Point out each leukocyte.
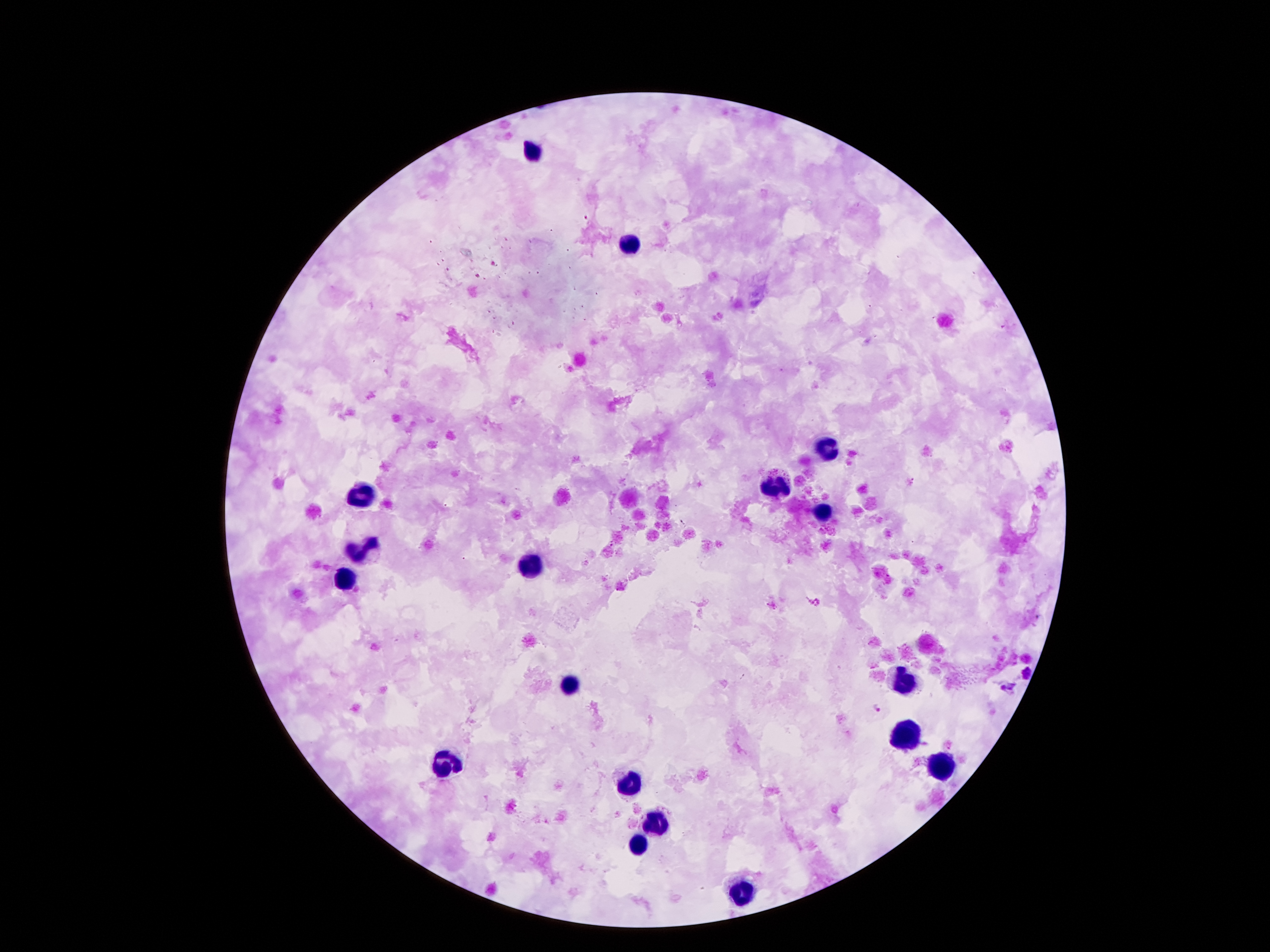

Approximate centers as {x, y} in pixels.
Leukocytes: {532, 152}, {628, 246}, {825, 453}, {775, 483}, {363, 496}, {821, 514}, {363, 551}, {532, 563}, {345, 580}, {907, 684}, {573, 686}, {903, 733}, {445, 762}, {944, 766}, {630, 783}, {654, 824}, {638, 844}, {741, 893}.

Plasmodium parasite locations: {585, 216}, {493, 263}, {477, 276}, {518, 490}, {445, 506}, {464, 558}, {812, 601}, {876, 709}. Thick blood film. Photographed through the microscope eyepiece with a smartphone camera. Image is 1270×952 pixels. One field from this slide. Giemsa-stained preparation. Patient malaria status: positive for Plasmodium falciparum. 100x magnification.